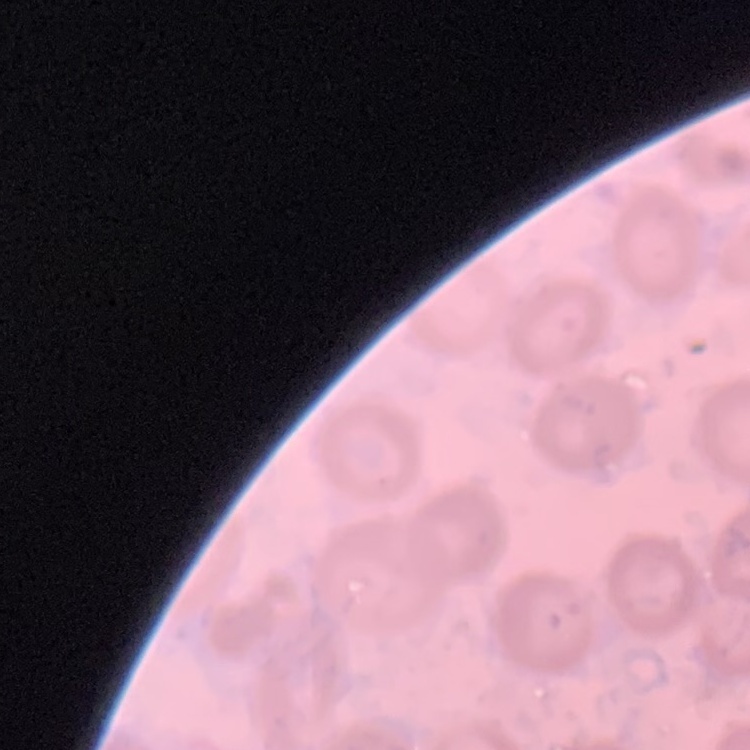
erythrocyte morphology = no rouleaux formation
preparation = thin blood smear
stain = Field's or Giemsa
image type = square crop of a larger photomicrograph